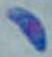

Summary:
  - Magnification: 1000x
  - Identification: Toxoplasma gondii
  - Modality: micrograph